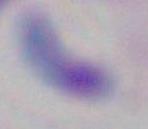
magnification: 1000x
identification: Toxoplasma gondii
modality: micrograph